Classify this cell by malaria status.
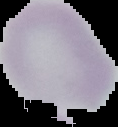

Uninfected.

Summary:
  - Image type: segmented cell region on a black background
  - Preparation: thin blood smear
  - Image size: 118×127 pixels